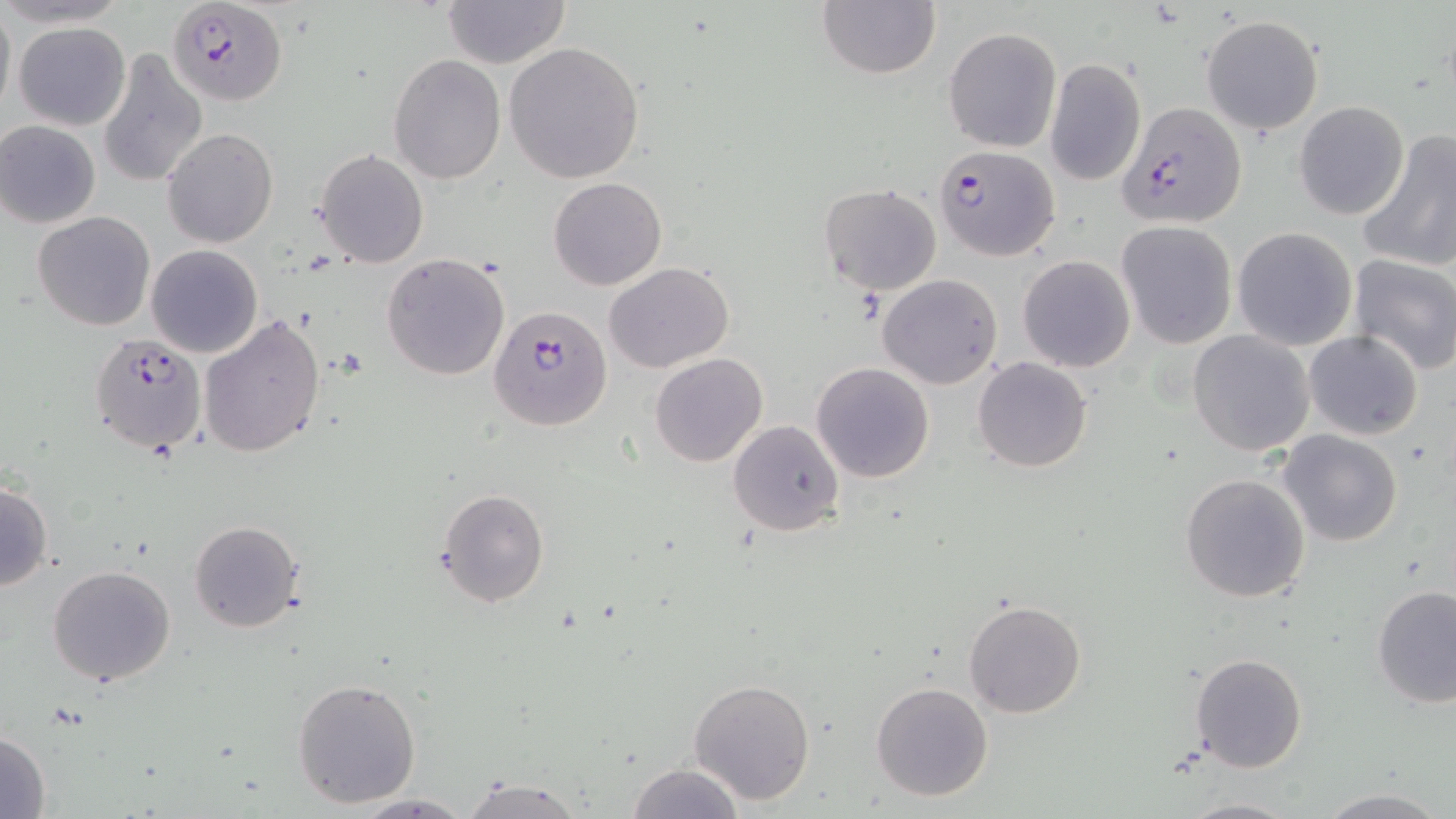
{
  "slide_level_diagnosis": "Plasmodium falciparum",
  "uninfected_red_blood_cell_locations": "approximate bounding boxes as named x1/y1/x2/y2 corners in pixels: (x1=440, y1=0, x2=571, y2=69), (x1=815, y1=1, x2=941, y2=80), (x1=0, y1=3, x2=15, y2=123), (x1=1200, y1=15, x2=1325, y2=136), (x1=13, y1=21, x2=131, y2=130), (x1=942, y1=26, x2=1063, y2=153), (x1=504, y1=41, x2=644, y2=183), (x1=97, y1=49, x2=208, y2=188), (x1=388, y1=55, x2=507, y2=185), (x1=1045, y1=58, x2=1146, y2=186), (x1=1294, y1=101, x2=1410, y2=220), (x1=1, y1=120, x2=101, y2=227), (x1=161, y1=127, x2=279, y2=248), (x1=1357, y1=131, x2=1456, y2=273), (x1=314, y1=149, x2=429, y2=267), (x1=548, y1=177, x2=667, y2=290), (x1=818, y1=183, x2=943, y2=296), (x1=33, y1=211, x2=157, y2=331), (x1=1116, y1=221, x2=1237, y2=349), (x1=1232, y1=227, x2=1358, y2=351), (x1=145, y1=245, x2=262, y2=357), (x1=381, y1=253, x2=510, y2=380), (x1=1347, y1=254, x2=1456, y2=375), (x1=1018, y1=255, x2=1135, y2=372), (x1=605, y1=262, x2=733, y2=373), (x1=877, y1=273, x2=1004, y2=389), (x1=198, y1=312, x2=326, y2=458), (x1=1188, y1=330, x2=1315, y2=458), (x1=1303, y1=331, x2=1425, y2=441), (x1=650, y1=352, x2=768, y2=466), (x1=972, y1=357, x2=1092, y2=472), (x1=810, y1=362, x2=935, y2=483), (x1=727, y1=419, x2=845, y2=536), (x1=1278, y1=430, x2=1402, y2=546), (x1=1180, y1=474, x2=1310, y2=605), (x1=0, y1=479, x2=53, y2=594), (x1=436, y1=489, x2=550, y2=608), (x1=189, y1=520, x2=304, y2=633), (x1=47, y1=564, x2=176, y2=686), (x1=1372, y1=585, x2=1456, y2=710), (x1=962, y1=600, x2=1087, y2=718), (x1=1189, y1=652, x2=1307, y2=772), (x1=292, y1=678, x2=422, y2=808), (x1=688, y1=678, x2=815, y2=805), (x1=870, y1=681, x2=993, y2=803), (x1=0, y1=730, x2=52, y2=817), (x1=627, y1=761, x2=746, y2=818), (x1=463, y1=775, x2=586, y2=819), (x1=1314, y1=790, x2=1450, y2=819), (x1=349, y1=794, x2=477, y2=818), (x1=1178, y1=796, x2=1300, y2=819)",
  "magnification": "1000x",
  "stain": "May-Grünwald-Giemsa",
  "plasmodium_falciparum_infected_red_blood_cell_locations": "approximate bounding boxes as named x1/y1/x2/y2 corners in pixels: (x1=167, y1=0, x2=288, y2=106), (x1=1117, y1=101, x2=1244, y2=227), (x1=934, y1=144, x2=1061, y2=262), (x1=489, y1=305, x2=613, y2=429), (x1=89, y1=332, x2=207, y2=458)",
  "field_of_view": "single",
  "image_size": "1456×819 pixels",
  "modality": "light microscopy",
  "preparation": "thin blood smear"
}